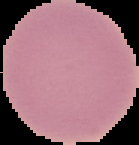
image size = 139×145 pixels
preparation = thin blood smear
image type = segmented cell region on a black background
malaria status = uninfected